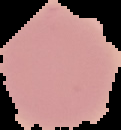
Malaria status: uninfected. From a thin blood film. Image is 121×130 pixels. Segmented cell region on a black background.